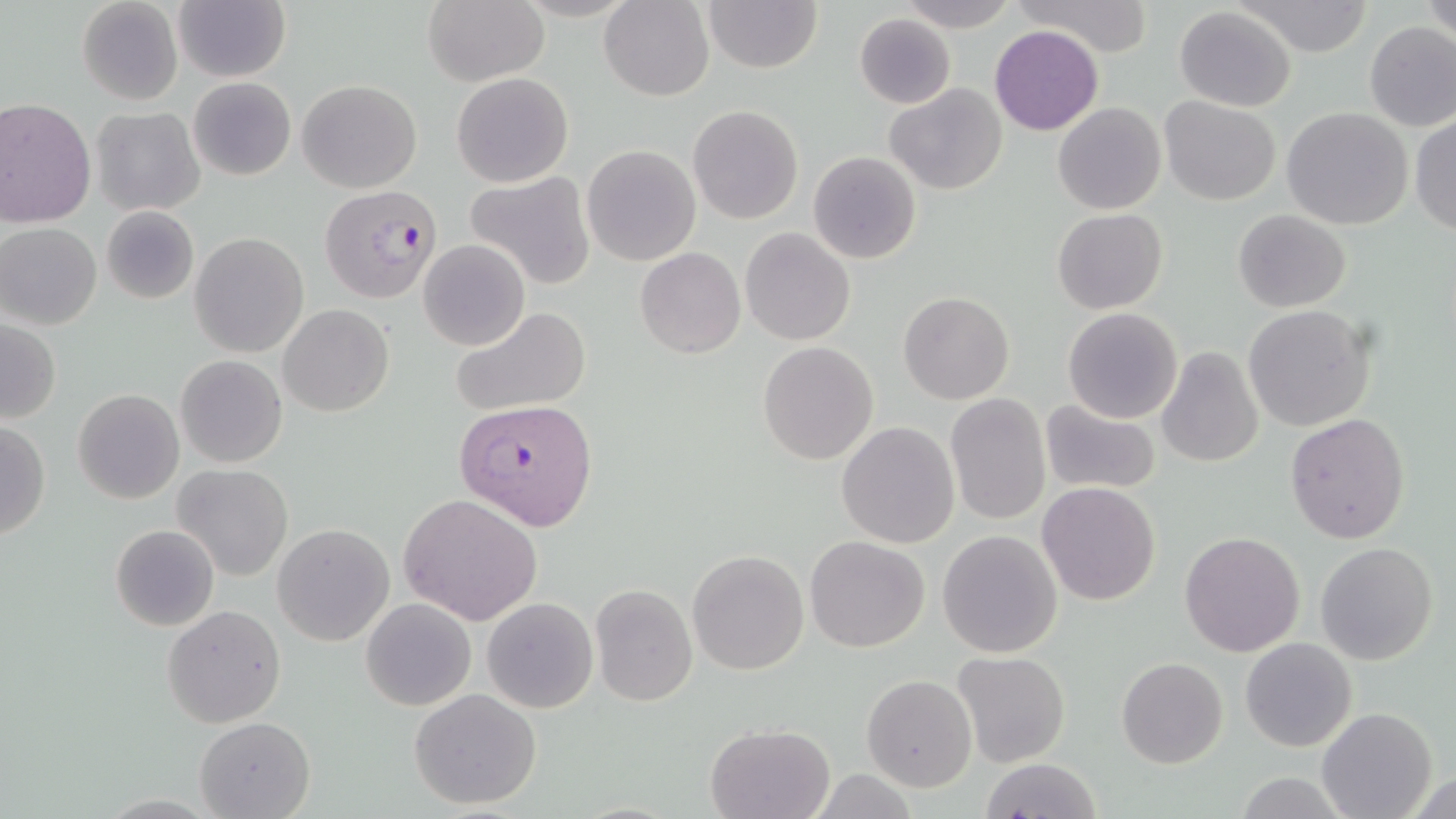
{
  "slide_level_diagnosis": "Plasmodium falciparum",
  "image_size": "1456×819 pixels",
  "modality": "light microscopy",
  "plasmodium_falciparum_infected_red_blood_cell_locations": "approximate bounding boxes as [x1, y1, x2, y2] in pixels: [319, 182, 441, 305], [456, 397, 598, 531]",
  "uninfected_red_blood_cell_locations": "approximate bounding boxes as [x1, y1, x2, y2] in pixels: [76, 0, 183, 106], [600, 0, 713, 101], [702, 0, 822, 73], [895, 0, 1017, 32], [1012, 0, 1155, 57], [1422, 0, 1455, 41], [174, 2, 289, 82], [423, 2, 547, 86], [1237, 2, 1374, 56], [1173, 6, 1298, 111], [855, 14, 956, 109], [1362, 21, 1456, 132], [989, 24, 1103, 135], [451, 72, 574, 188], [189, 77, 295, 181], [296, 79, 422, 193], [885, 83, 1008, 196], [1160, 96, 1282, 205], [0, 99, 96, 227], [1053, 102, 1166, 215], [687, 104, 804, 224], [90, 106, 205, 217], [1282, 107, 1413, 231], [1409, 113, 1456, 237], [581, 144, 701, 267], [807, 150, 923, 264], [465, 172, 596, 289], [101, 205, 199, 303], [1051, 208, 1168, 314], [1232, 208, 1352, 312], [0, 223, 102, 331], [740, 227, 855, 346], [189, 233, 309, 357], [418, 240, 530, 352], [636, 247, 745, 359], [897, 290, 1014, 404], [279, 304, 394, 416], [1244, 304, 1375, 433], [451, 307, 592, 418], [1062, 307, 1183, 424], [1, 319, 60, 424], [757, 341, 880, 466], [1156, 346, 1264, 466], [176, 354, 287, 468], [72, 389, 184, 504], [944, 393, 1051, 525], [1040, 402, 1162, 496], [1284, 411, 1410, 544], [0, 420, 51, 540], [836, 421, 960, 549], [173, 464, 293, 581], [1036, 482, 1162, 604], [399, 492, 544, 627], [110, 524, 220, 632], [273, 524, 394, 646], [938, 530, 1063, 657], [1178, 532, 1305, 658], [805, 536, 931, 654], [1315, 542, 1438, 664], [687, 549, 809, 675], [590, 583, 697, 707], [360, 597, 478, 711], [482, 597, 597, 713], [162, 604, 285, 728], [1240, 636, 1358, 752], [952, 651, 1071, 767], [1115, 656, 1228, 768], [862, 675, 977, 792], [409, 688, 543, 810], [1316, 707, 1437, 819], [194, 717, 314, 818], [706, 723, 834, 819], [978, 758, 1104, 818], [1406, 771, 1454, 819], [1232, 772, 1353, 817]",
  "stain": "May-Grünwald-Giemsa",
  "magnification": "1000x",
  "field_of_view": "single",
  "preparation": "thin blood smear"
}